Locate and identify every blood parasite.
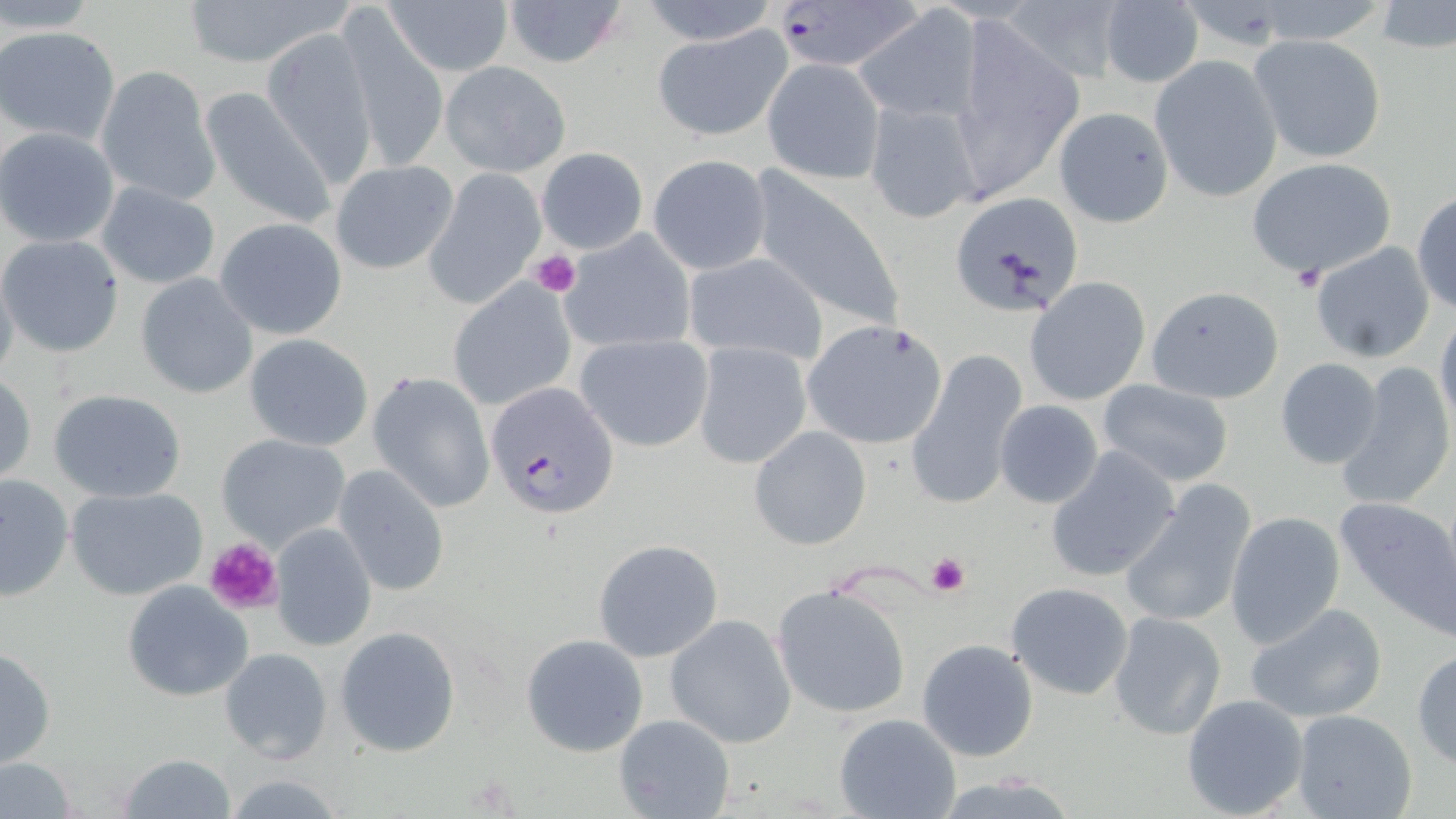

Approximate bounding boxes as [x1, y1, x2, y2] in pixels.
Plasmodium falciparum-infected red blood cells: [774, 1, 929, 72], [488, 381, 620, 519].
No Plasmodium ovale, Plasmodium malariae, Plasmodium vivax, Babesia divergens, or Trypanosoma brucei observed.

Uninfected red blood cell locations: [178, 0, 350, 68], [499, 0, 631, 69], [638, 0, 779, 44], [998, 0, 1132, 85], [1373, 1, 1456, 56], [383, 2, 514, 78], [1097, 2, 1204, 87], [887, 5, 1046, 152], [854, 7, 981, 125], [338, 13, 449, 175], [950, 15, 1084, 197], [650, 25, 792, 142], [1, 26, 121, 147], [262, 27, 380, 189], [1248, 34, 1388, 164], [1150, 55, 1283, 202], [761, 57, 886, 184], [439, 60, 571, 178], [92, 67, 218, 204], [197, 84, 335, 229], [865, 98, 985, 226], [1052, 106, 1174, 228], [0, 128, 120, 248], [535, 147, 649, 255], [648, 154, 772, 276], [1246, 157, 1396, 280], [328, 161, 460, 275], [748, 168, 909, 337], [424, 170, 546, 310], [94, 182, 221, 290], [1411, 190, 1456, 314], [950, 191, 1085, 316], [215, 218, 347, 340], [559, 229, 697, 355], [0, 234, 126, 358], [1310, 239, 1436, 363], [681, 251, 828, 366], [0, 268, 20, 387], [134, 273, 260, 398], [1024, 277, 1151, 406], [448, 278, 577, 411], [1146, 285, 1284, 404], [1434, 309, 1456, 436], [801, 318, 949, 450], [244, 333, 374, 452], [575, 333, 713, 453], [692, 341, 813, 469], [908, 349, 1028, 506], [1274, 357, 1383, 468], [1338, 362, 1455, 512], [367, 371, 495, 513], [1, 372, 36, 486], [1097, 378, 1234, 488], [46, 388, 189, 503], [993, 399, 1106, 510], [748, 425, 871, 550], [216, 434, 349, 549], [1045, 444, 1183, 582], [333, 465, 449, 596], [0, 473, 73, 601], [1121, 481, 1257, 628], [65, 485, 208, 601], [1333, 493, 1456, 632], [1223, 510, 1346, 651], [267, 522, 378, 651], [592, 538, 724, 662], [122, 579, 255, 702], [1005, 581, 1135, 701], [772, 583, 911, 718], [1243, 601, 1389, 725], [1108, 610, 1227, 742], [665, 614, 797, 748], [335, 625, 461, 758], [520, 632, 649, 757], [916, 638, 1039, 762], [0, 645, 55, 770], [219, 647, 333, 763], [1412, 647, 1456, 768], [1180, 693, 1310, 817], [1291, 709, 1418, 819], [833, 713, 961, 819], [614, 714, 735, 819], [115, 753, 236, 818], [0, 755, 82, 818]. Platelet locations: [529, 250, 581, 297], [1288, 266, 1325, 294], [203, 537, 283, 616], [925, 552, 969, 597]. Slide-level diagnosis: Plasmodium falciparum. Light microscopy. May-Grünwald-Giemsa stain. 1000x magnification. Image is 1456×819 pixels. One field of a larger specimen. Thin blood film.